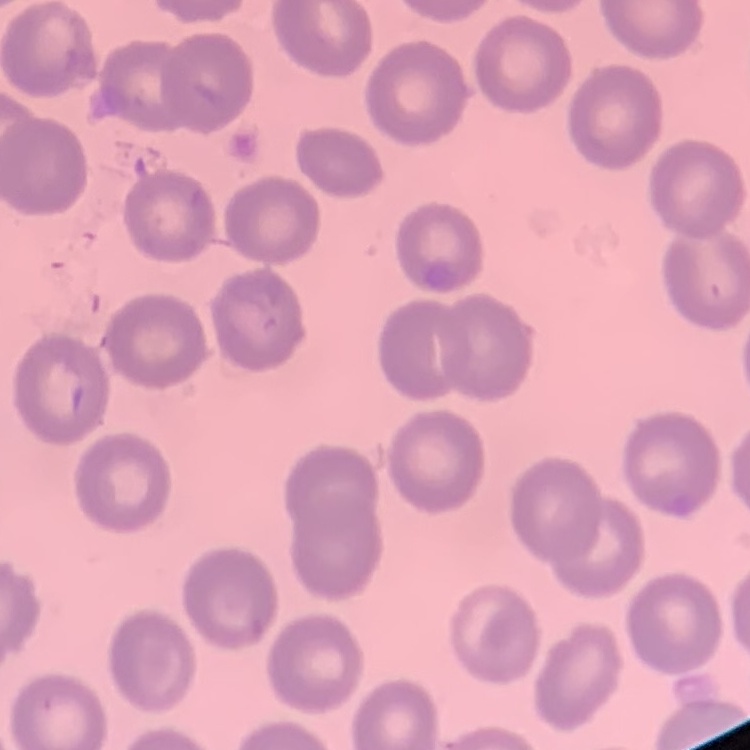
erythrocyte_morphology: no rouleaux formation
image_type: square crop of a larger photomicrograph
preparation: thin peripheral smear
stain: Field's or Giemsa